Comment on the morphology of the erythrocytes.
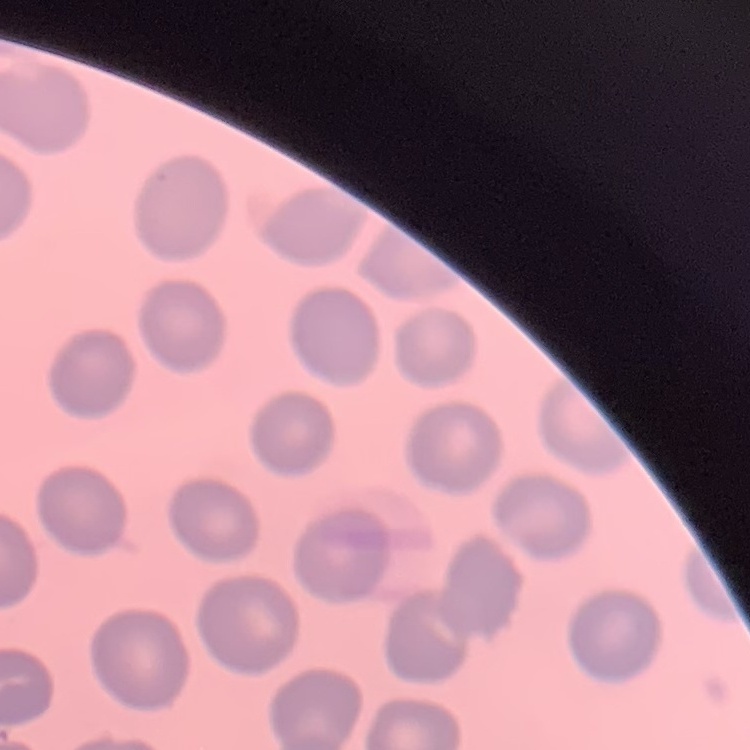

No rouleaux formation.

Thin blood film. Field's or Giemsa stain. Square crop of a larger photomicrograph.